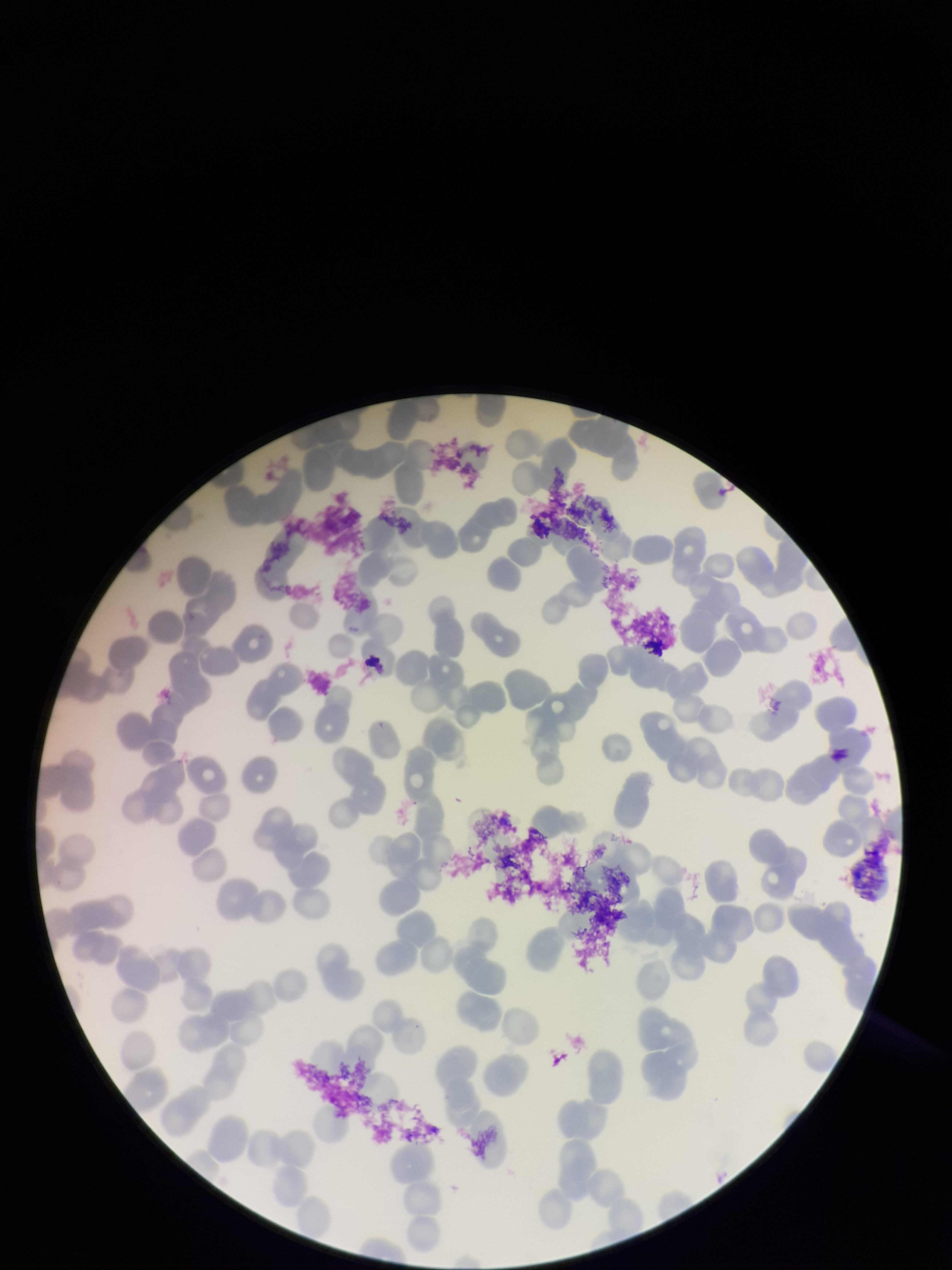 Single field of view. Giemsa stain. Species reported for this patient: Plasmodium falciparum. Red blood cell count: 160. Preparation: thin blood smear. Parasitized red blood cells: none seen. Parasitized red blood cell count: 0. Patient malaria status: infected. Image is 952×1270 pixels. Photographed through the microscope eyepiece with a smartphone camera.